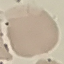
malaria status = uninfected
image type = automatically extracted cell patch, resized to 64 × 64 pixels
capture = smartphone through the microscope eyepiece
stain = Giemsa
preparation = thin blood film